Identify the blood parasite species.
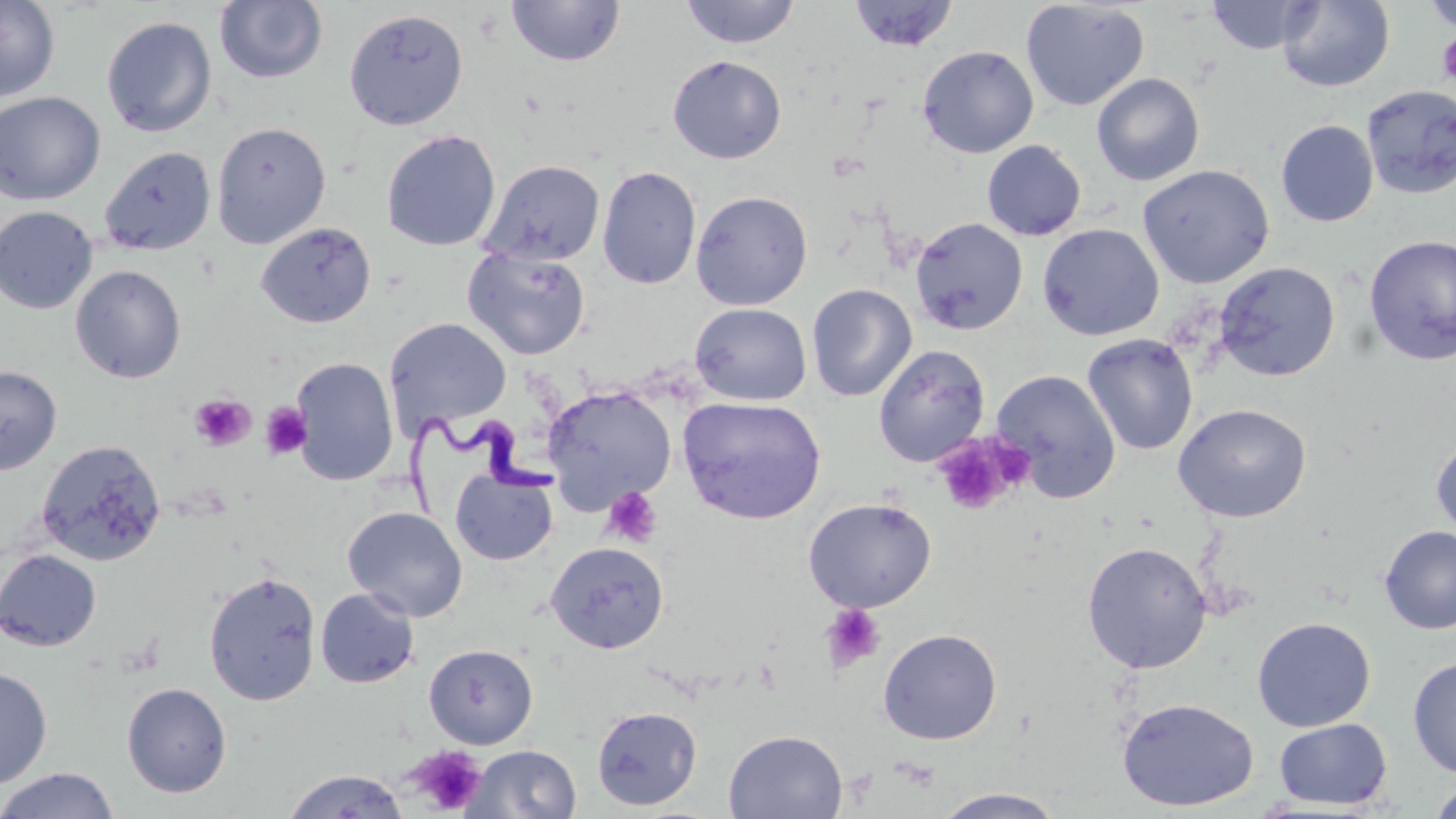

Trypanosoma brucei.

{
  "preparation": "thin blood film",
  "trypanosoma_brucei_locations": "approximate bounding boxes as [x1, y1, x2, y2] in pixels: [405, 407, 560, 521]",
  "magnification": "1000x",
  "uninfected_red_blood_cell_locations": "approximate bounding boxes as [x1, y1, x2, y2] in pixels: [0, 0, 60, 104], [680, 0, 801, 49], [1204, 0, 1321, 55], [1420, 0, 1456, 33], [214, 1, 328, 84], [506, 1, 625, 67], [847, 1, 959, 53], [1020, 1, 1150, 112], [1277, 1, 1395, 92], [344, 8, 469, 130], [101, 16, 217, 137], [917, 45, 1039, 158], [667, 55, 787, 164], [1091, 72, 1205, 186], [1361, 84, 1456, 199], [0, 91, 106, 206], [1275, 119, 1378, 226], [211, 121, 331, 249], [381, 130, 501, 251], [982, 139, 1086, 241], [99, 146, 217, 256], [480, 159, 606, 267], [1137, 163, 1274, 289], [597, 165, 701, 290], [690, 190, 813, 310], [0, 206, 98, 314], [910, 216, 1028, 335], [255, 223, 376, 328], [1037, 223, 1164, 341], [1363, 234, 1456, 365], [462, 246, 591, 360], [1214, 262, 1341, 382], [70, 264, 187, 383], [806, 283, 917, 402], [689, 302, 812, 406], [383, 317, 512, 434], [1082, 333, 1199, 456], [873, 344, 991, 467], [290, 357, 398, 486], [0, 365, 62, 475], [991, 369, 1122, 503], [542, 386, 677, 513], [678, 396, 827, 525], [1172, 403, 1311, 523], [1431, 435, 1456, 542], [37, 438, 166, 566], [451, 469, 558, 565], [803, 497, 937, 612], [343, 506, 468, 621], [1378, 525, 1456, 635], [545, 541, 669, 654], [1081, 541, 1213, 674], [0, 549, 102, 651], [203, 570, 322, 706], [315, 588, 419, 689], [1252, 616, 1376, 731], [878, 627, 1003, 745], [424, 643, 538, 748], [1407, 657, 1456, 778], [0, 665, 52, 789], [122, 682, 232, 797], [1116, 697, 1259, 812], [591, 705, 702, 810], [1273, 717, 1392, 810], [724, 729, 848, 819], [466, 744, 582, 818], [0, 767, 120, 819], [280, 769, 411, 818], [1426, 779, 1456, 819], [932, 787, 1067, 818]",
  "platelet_locations": "approximate bounding boxes as [x1, y1, x2, y2] in pixels: [1437, 32, 1456, 87], [189, 393, 255, 451], [260, 403, 311, 460], [933, 432, 1028, 516], [601, 487, 662, 548], [820, 604, 887, 674], [405, 745, 487, 816]",
  "field_of_view": "single",
  "stain": "May-Grünwald-Giemsa",
  "image_size": "1456×819 pixels",
  "modality": "light microscopy"
}